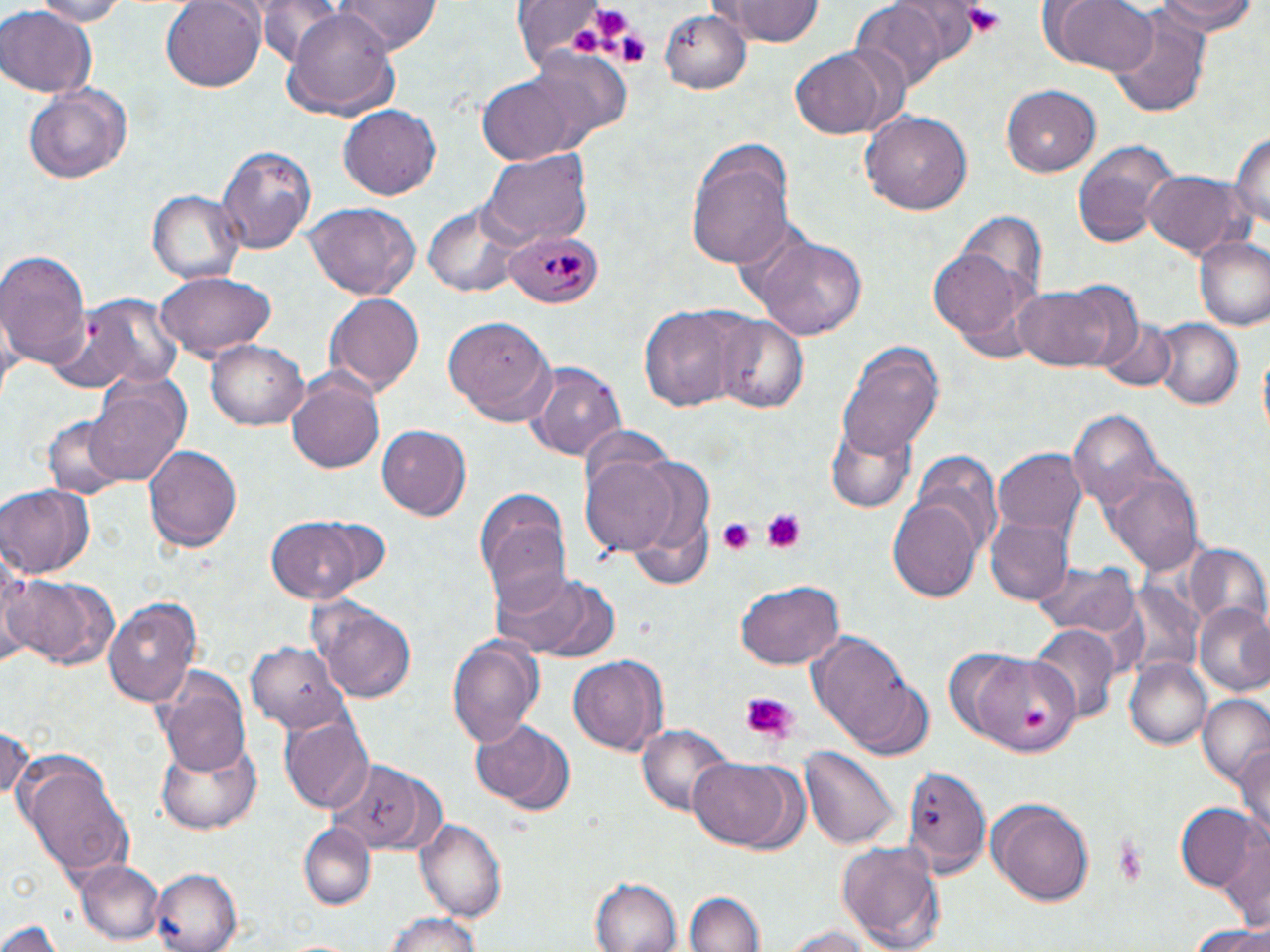

Summary:
  - Coordinate format: approximate bounding boxes as (x1,y1)-(x2,y2) corner pairs in pixels
  - Plasmodium malariae-infected red blood cell locations: (503,228)-(603,308)
  - Uninfected red blood cell locations: (28,0)-(130,25), (162,0)-(264,92), (335,0)-(443,52), (1048,0)-(1159,75), (1154,0)-(1257,36), (719,2)-(827,47), (850,2)-(947,91), (282,3)-(401,116), (509,3)-(623,72), (0,7)-(96,96), (659,7)-(750,97), (1110,11)-(1211,116), (787,46)-(907,141), (523,52)-(632,147), (475,73)-(583,166), (24,82)-(135,187), (1002,84)-(1102,176), (339,105)-(437,201), (859,109)-(972,216), (1230,126)-(1269,243), (1070,142)-(1177,248), (686,143)-(797,268), (216,144)-(315,256), (479,147)-(593,246), (1141,170)-(1244,259), (147,188)-(245,286), (422,199)-(524,299), (302,203)-(421,300), (959,213)-(1047,303), (744,230)-(869,342), (1193,234)-(1270,333), (929,244)-(1038,356), (0,247)-(90,372), (154,271)-(278,362), (1015,285)-(1121,373), (324,292)-(424,398), (52,293)-(184,394), (641,305)-(741,412), (708,313)-(811,415), (446,314)-(557,425), (1152,318)-(1244,410), (1095,319)-(1177,392), (206,340)-(309,432), (838,341)-(943,461), (524,362)-(627,462), (287,373)-(386,474), (82,381)-(189,491), (1070,409)-(1162,506), (42,413)-(133,499), (828,423)-(917,514), (376,425)-(469,521), (143,444)-(243,554), (994,449)-(1086,541), (913,451)-(1003,556), (581,452)-(681,557), (1105,465)-(1204,574), (0,485)-(96,579), (474,491)-(571,606), (889,499)-(981,602), (986,516)-(1073,605), (268,518)-(367,602), (1184,547)-(1270,638), (0,553)-(39,669), (1033,561)-(1139,638), (491,570)-(619,661), (11,573)-(122,672), (735,581)-(846,671), (103,598)-(203,707), (311,600)-(418,701), (1195,602)-(1270,696), (1031,626)-(1120,723), (805,632)-(929,756), (446,634)-(545,748), (246,642)-(347,731), (966,651)-(1077,755), (567,654)-(669,756), (1124,660)-(1213,750), (151,663)-(254,773), (1197,696)-(1270,789), (282,717)-(373,812), (0,721)-(32,807), (471,722)-(577,817), (639,722)-(733,817), (155,734)-(261,833), (1234,743)-(1270,846), (801,744)-(899,849), (687,755)-(796,850), (21,761)-(137,884), (326,761)-(438,853), (903,766)-(990,877), (989,799)-(1092,908), (1175,803)-(1259,892), (415,815)-(509,921), (300,825)-(373,909), (1220,830)-(1269,934), (839,840)-(945,952), (76,859)-(165,945), (151,869)-(241,952), (590,877)-(681,951), (682,890)-(764,952), (380,912)-(488,952), (2,919)-(62,951), (1185,920)-(1270,951), (779,924)-(884,951), (280,936)-(359,952)
  - Platelet locations: (960,2)-(1007,37), (592,8)-(632,39), (570,28)-(602,58), (615,33)-(649,66), (760,508)-(807,554), (716,518)-(756,553), (739,692)-(797,745), (1025,708)-(1049,734), (1109,834)-(1154,886)
  - Slide-level diagnosis: Plasmodium malariae
  - Preparation: thin blood smear
  - Modality: light microscopy
  - Field of view: one of a larger specimen
  - Magnification: 1000x
  - Stain: May-Grünwald-Giemsa
  - Image size: 1270×952 pixels